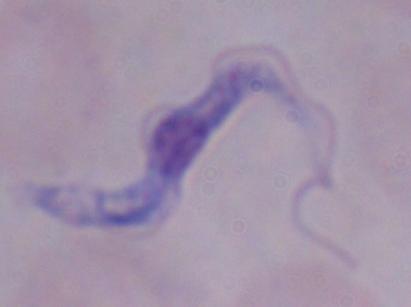
magnification = 1000x
modality = micrograph
identification = trypanosome